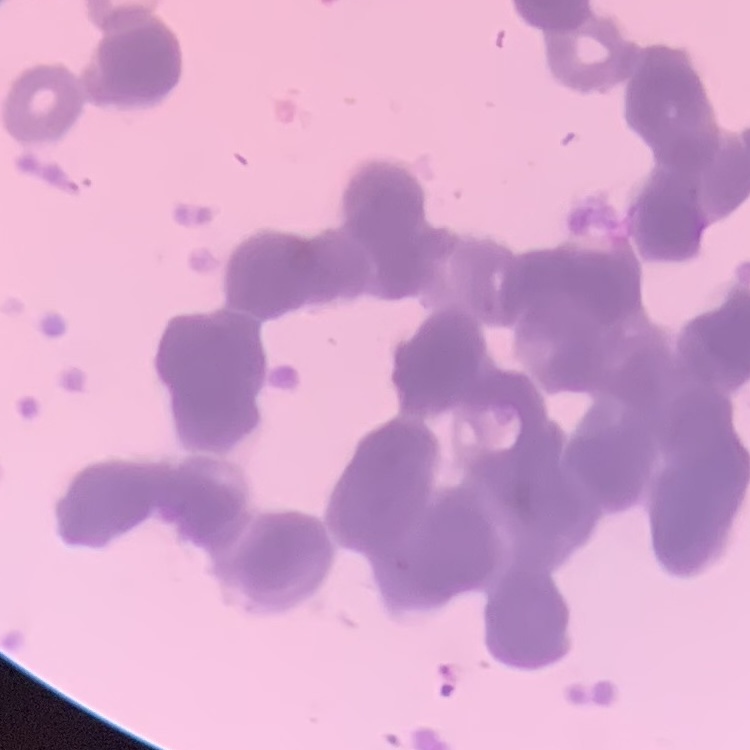

Summary:
  - Erythrocyte morphology: rouleaux formation
  - Image type: square crop of a larger photomicrograph
  - Preparation: thin blood film
  - Stain: Field's or Giemsa